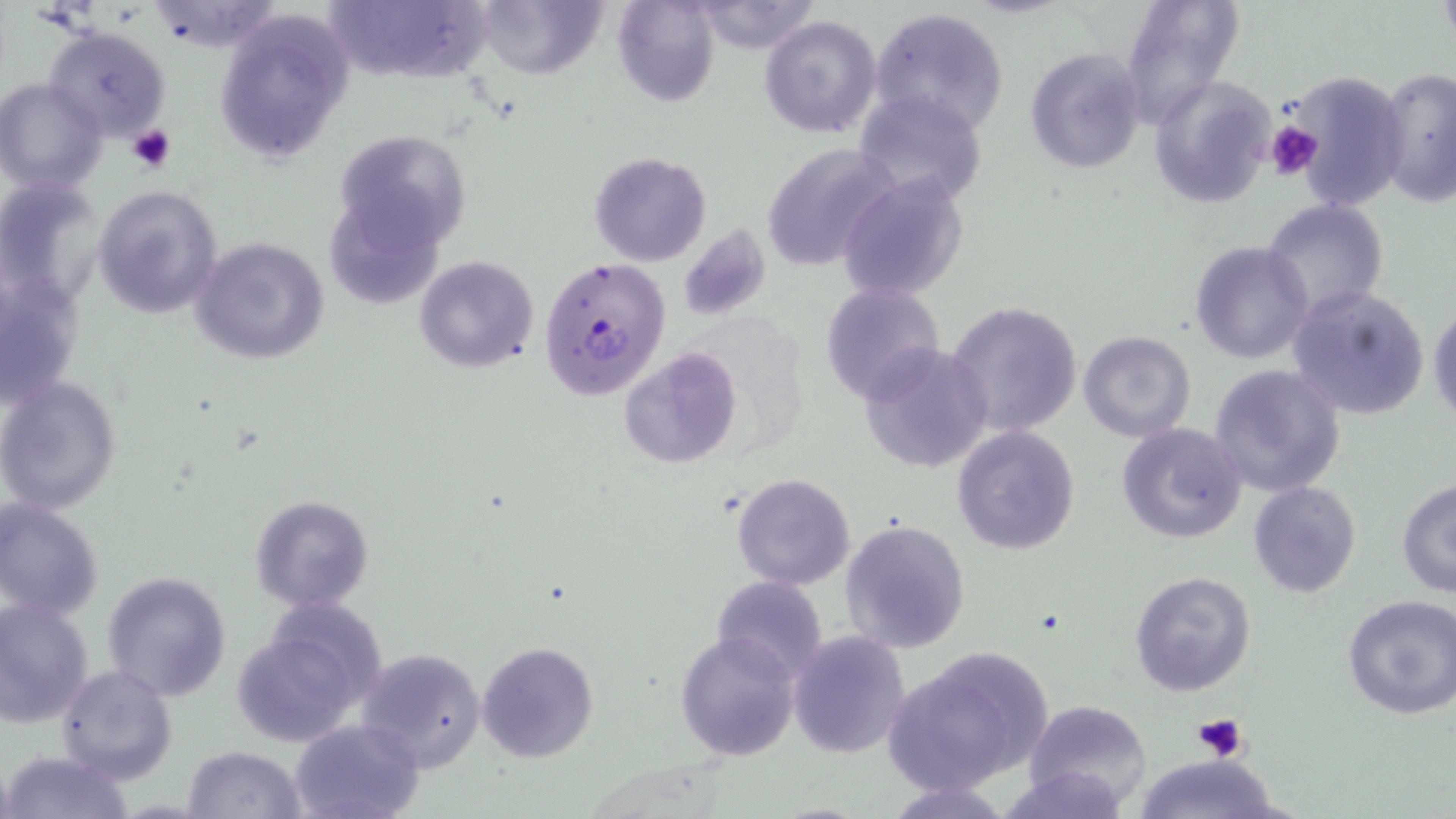 Approximate bounding boxes as (x1, y1, x2, y2) in pixels. Uninfected red blood cell locations: (325, 0, 488, 82), (470, 0, 607, 80), (612, 0, 721, 108), (1119, 0, 1244, 127), (687, 1, 823, 54), (869, 7, 1010, 135), (212, 11, 354, 168), (759, 14, 883, 139), (43, 25, 172, 142), (1025, 48, 1145, 172), (1373, 66, 1456, 211), (1278, 70, 1410, 212), (1148, 74, 1276, 208), (0, 78, 108, 196), (851, 87, 988, 206), (333, 125, 474, 257), (759, 144, 898, 271), (588, 151, 712, 266), (0, 175, 104, 305), (837, 175, 970, 302), (92, 184, 224, 320), (1261, 199, 1389, 321), (675, 224, 772, 322), (189, 235, 333, 366), (1188, 240, 1315, 365), (414, 255, 539, 374), (0, 273, 85, 411), (819, 282, 946, 402), (1286, 284, 1431, 420), (943, 300, 1085, 438), (1427, 302, 1456, 427), (1078, 330, 1196, 441), (857, 343, 992, 474), (618, 348, 743, 469), (1209, 363, 1347, 497), (0, 376, 123, 515), (1116, 421, 1247, 544), (952, 424, 1079, 556), (730, 472, 857, 591), (1395, 479, 1456, 598), (1247, 481, 1362, 599), (250, 495, 375, 612), (0, 498, 104, 621), (839, 518, 971, 656), (102, 569, 232, 703), (1129, 571, 1257, 697), (710, 577, 829, 680), (1338, 595, 1456, 719), (0, 597, 95, 727), (234, 608, 385, 750), (675, 630, 799, 761), (786, 630, 911, 759), (477, 640, 599, 764), (883, 645, 1053, 796), (356, 646, 487, 772), (57, 664, 176, 784), (1025, 700, 1150, 809), (289, 717, 426, 819), (182, 745, 305, 819), (2, 748, 133, 819), (1129, 753, 1290, 819), (879, 778, 1017, 818). Platelet locations: (1265, 122, 1324, 180), (127, 124, 176, 172), (1194, 712, 1249, 764). Plasmodium falciparum-infected red blood cell locations: (537, 256, 671, 400). Slide-level diagnosis: Plasmodium falciparum. One field of a larger specimen. May-Grünwald-Giemsa-stained preparation. Captured at 1000x magnification. Light microscopy. Thin blood smear. Image is 1456×819 pixels.